Locate and identify every blood parasite.
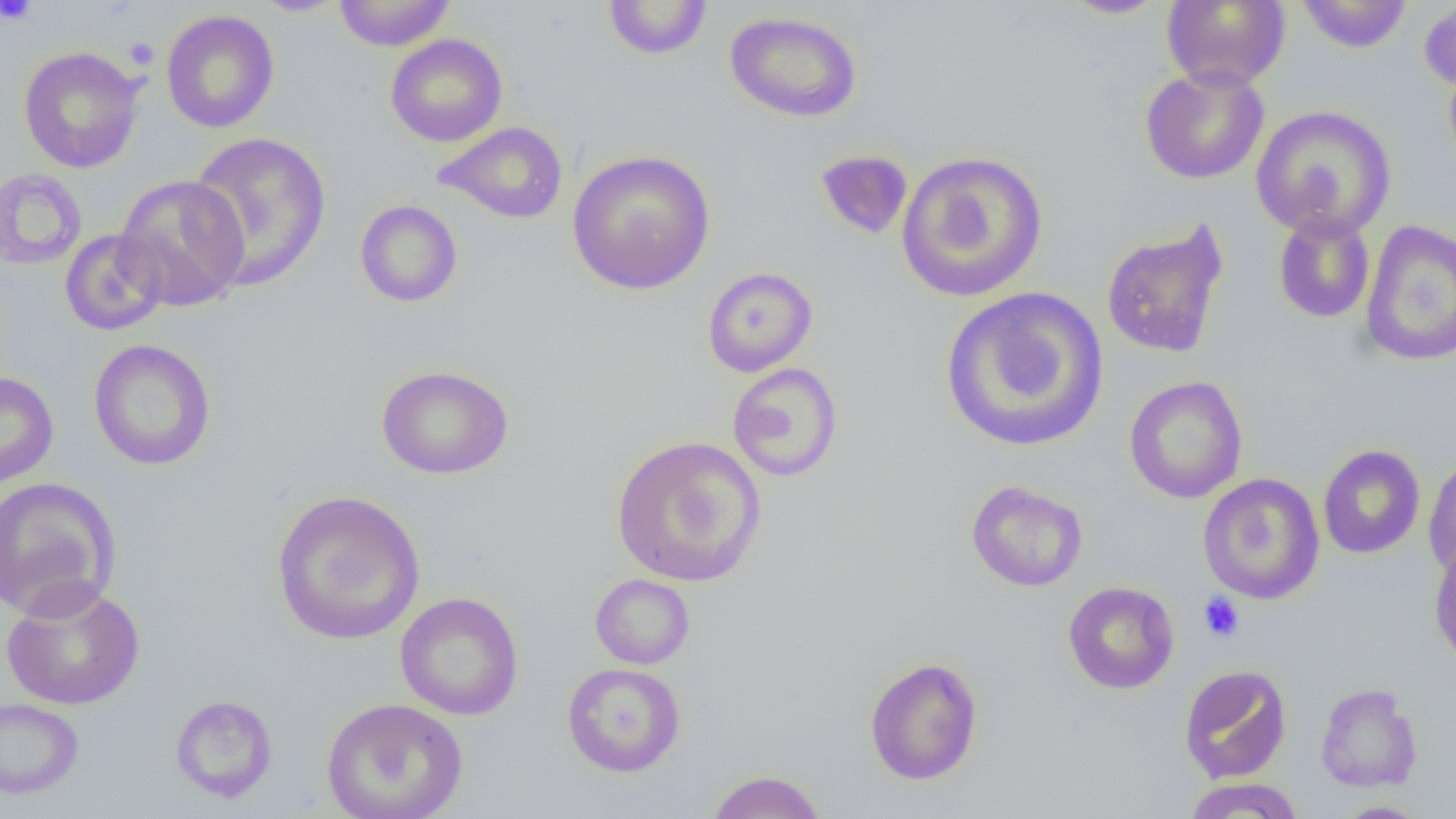

No blood parasites observed.

Summary:
  - Coordinate format: approximate bounding boxes as named x1/y1/x2/y2 corners in pixels
  - Platelet locations: (x1=1, y1=0, x2=37, y2=25), (x1=123, y1=36, x2=159, y2=70), (x1=1198, y1=592, x2=1244, y2=643)
  - Uninfected red blood cell locations: (x1=333, y1=0, x2=456, y2=51), (x1=1059, y1=0, x2=1170, y2=19), (x1=1161, y1=0, x2=1291, y2=89), (x1=1296, y1=0, x2=1413, y2=54), (x1=1418, y1=0, x2=1456, y2=93), (x1=250, y1=1, x2=349, y2=16), (x1=602, y1=1, x2=714, y2=60), (x1=161, y1=9, x2=280, y2=133), (x1=724, y1=12, x2=862, y2=123), (x1=385, y1=33, x2=508, y2=147), (x1=18, y1=46, x2=145, y2=173), (x1=1139, y1=64, x2=1270, y2=185), (x1=1250, y1=105, x2=1397, y2=240), (x1=434, y1=121, x2=568, y2=224), (x1=187, y1=131, x2=332, y2=291), (x1=814, y1=149, x2=913, y2=240), (x1=566, y1=150, x2=716, y2=295), (x1=896, y1=150, x2=1049, y2=303), (x1=0, y1=168, x2=88, y2=270), (x1=113, y1=174, x2=250, y2=311), (x1=355, y1=200, x2=463, y2=307), (x1=1273, y1=211, x2=1376, y2=324), (x1=1359, y1=219, x2=1456, y2=367), (x1=1101, y1=220, x2=1229, y2=360), (x1=59, y1=229, x2=170, y2=336), (x1=702, y1=266, x2=817, y2=377), (x1=941, y1=286, x2=1109, y2=454), (x1=88, y1=339, x2=216, y2=471), (x1=727, y1=362, x2=843, y2=482), (x1=376, y1=364, x2=514, y2=480), (x1=0, y1=372, x2=58, y2=488), (x1=1123, y1=375, x2=1248, y2=504), (x1=611, y1=435, x2=767, y2=587), (x1=1317, y1=444, x2=1426, y2=559), (x1=1423, y1=455, x2=1456, y2=581), (x1=1198, y1=472, x2=1325, y2=605), (x1=0, y1=477, x2=121, y2=622), (x1=966, y1=480, x2=1088, y2=592), (x1=271, y1=489, x2=426, y2=645), (x1=1429, y1=538, x2=1456, y2=670), (x1=590, y1=574, x2=695, y2=669), (x1=0, y1=581, x2=146, y2=711), (x1=1063, y1=581, x2=1179, y2=694), (x1=395, y1=591, x2=524, y2=721), (x1=864, y1=656, x2=983, y2=786), (x1=562, y1=662, x2=685, y2=777), (x1=1178, y1=664, x2=1292, y2=783), (x1=1315, y1=683, x2=1423, y2=793), (x1=170, y1=694, x2=278, y2=803), (x1=321, y1=697, x2=468, y2=819), (x1=0, y1=698, x2=84, y2=799), (x1=705, y1=769, x2=827, y2=819), (x1=1183, y1=777, x2=1304, y2=818), (x1=1332, y1=802, x2=1431, y2=819)
  - Slide-level diagnosis: no evidence of blood parasites
  - Preparation: thin blood film
  - Magnification: 1000x
  - Modality: optical microscopy
  - Image size: 1456×819 pixels
  - Field of view: one of a larger specimen